Locate every blood parasite and identify its species.
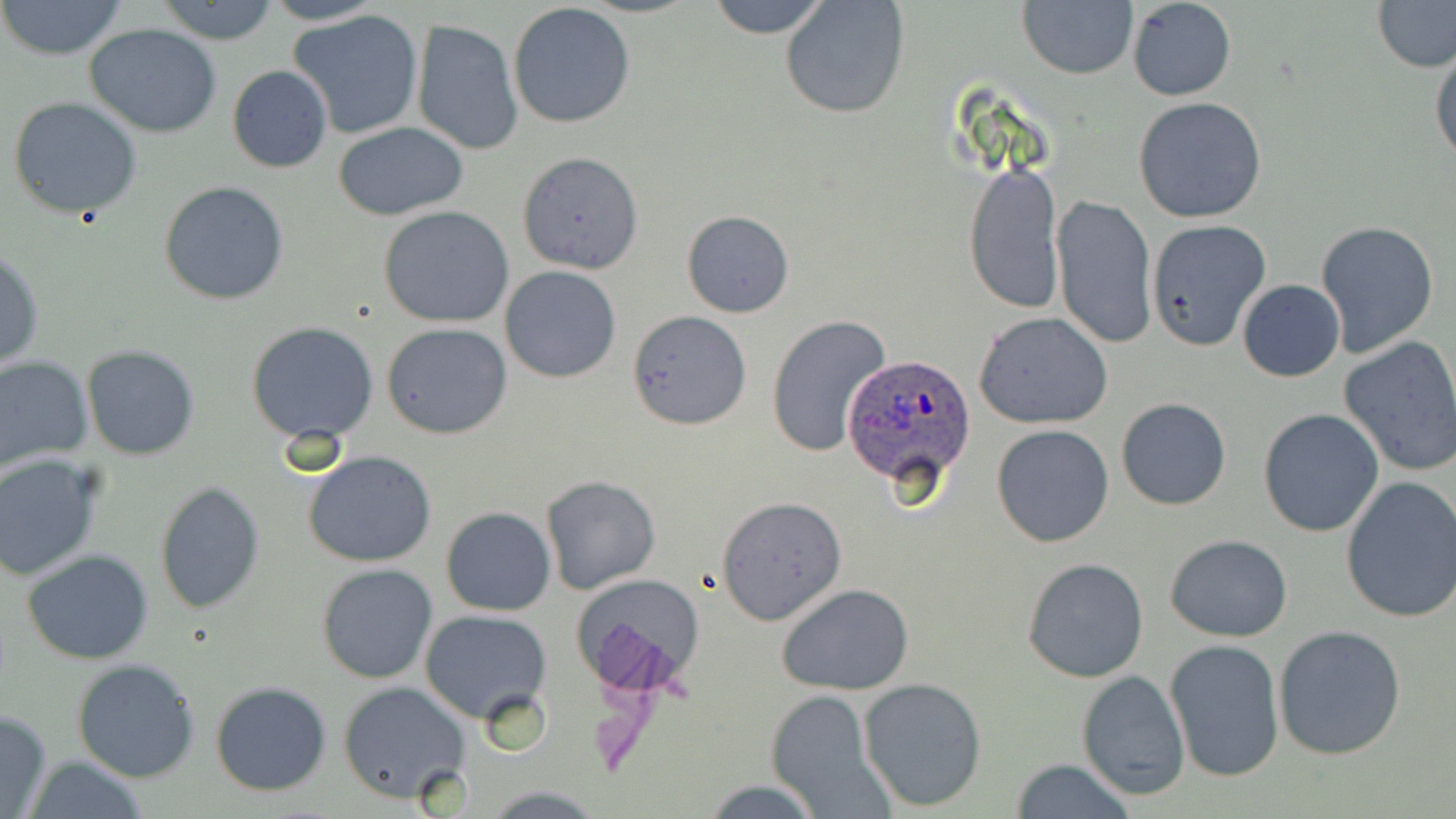

Approximate bounding boxes as named x1/y1/x2/y2 corners in pixels.
Plasmodium ovale-infected red blood cells: (x1=843, y1=351, x2=977, y2=494).
No Plasmodium falciparum, Plasmodium malariae, Plasmodium vivax, Babesia divergens, or Trypanosoma brucei observed.

Summary:
  - Uninfected red blood cell locations: (x1=0, y1=0, x2=127, y2=62), (x1=155, y1=0, x2=281, y2=44), (x1=259, y1=0, x2=389, y2=25), (x1=708, y1=0, x2=829, y2=39), (x1=780, y1=0, x2=910, y2=120), (x1=1374, y1=0, x2=1456, y2=72), (x1=1126, y1=1, x2=1237, y2=100), (x1=1017, y1=2, x2=1138, y2=80), (x1=508, y1=3, x2=636, y2=129), (x1=288, y1=8, x2=425, y2=140), (x1=413, y1=19, x2=522, y2=155), (x1=84, y1=24, x2=224, y2=136), (x1=1430, y1=45, x2=1456, y2=167), (x1=227, y1=65, x2=333, y2=174), (x1=8, y1=96, x2=143, y2=219), (x1=1133, y1=96, x2=1268, y2=224), (x1=332, y1=120, x2=469, y2=220), (x1=516, y1=151, x2=643, y2=274), (x1=963, y1=161, x2=1063, y2=313), (x1=159, y1=181, x2=290, y2=303), (x1=1052, y1=194, x2=1157, y2=348), (x1=379, y1=205, x2=514, y2=328), (x1=682, y1=210, x2=795, y2=317), (x1=1145, y1=219, x2=1271, y2=350), (x1=1314, y1=219, x2=1439, y2=359), (x1=0, y1=249, x2=44, y2=370), (x1=501, y1=266, x2=620, y2=382), (x1=1237, y1=280, x2=1345, y2=382), (x1=627, y1=309, x2=752, y2=430), (x1=973, y1=312, x2=1114, y2=429), (x1=767, y1=314, x2=894, y2=460), (x1=247, y1=322, x2=380, y2=445), (x1=381, y1=322, x2=512, y2=439), (x1=1339, y1=337, x2=1456, y2=476), (x1=81, y1=345, x2=200, y2=461), (x1=0, y1=355, x2=93, y2=471), (x1=1115, y1=397, x2=1232, y2=510), (x1=1258, y1=409, x2=1384, y2=537), (x1=991, y1=423, x2=1115, y2=548), (x1=303, y1=450, x2=438, y2=567), (x1=0, y1=454, x2=106, y2=580), (x1=542, y1=475, x2=661, y2=595), (x1=1339, y1=476, x2=1456, y2=625), (x1=154, y1=482, x2=265, y2=612), (x1=717, y1=498, x2=845, y2=626), (x1=441, y1=506, x2=555, y2=616), (x1=1165, y1=535, x2=1292, y2=640), (x1=22, y1=549, x2=154, y2=663), (x1=1022, y1=557, x2=1150, y2=683), (x1=317, y1=563, x2=437, y2=683), (x1=573, y1=574, x2=706, y2=695), (x1=776, y1=584, x2=914, y2=695), (x1=420, y1=609, x2=552, y2=723), (x1=1274, y1=626, x2=1407, y2=761), (x1=1164, y1=637, x2=1285, y2=780), (x1=72, y1=659, x2=201, y2=783), (x1=1077, y1=668, x2=1191, y2=799), (x1=858, y1=677, x2=988, y2=811), (x1=210, y1=680, x2=332, y2=795), (x1=338, y1=681, x2=474, y2=804), (x1=764, y1=690, x2=890, y2=816), (x1=0, y1=708, x2=52, y2=819), (x1=19, y1=756, x2=152, y2=818), (x1=1008, y1=759, x2=1137, y2=819), (x1=697, y1=779, x2=830, y2=818), (x1=480, y1=783, x2=604, y2=817)
  - Slide-level diagnosis: Plasmodium ovale
  - Image size: 1456×819 pixels
  - Magnification: 1000x
  - Field of view: single
  - Modality: light microscopy
  - Preparation: thin blood film
  - Stain: May-Grünwald-Giemsa